Identify the parasite.
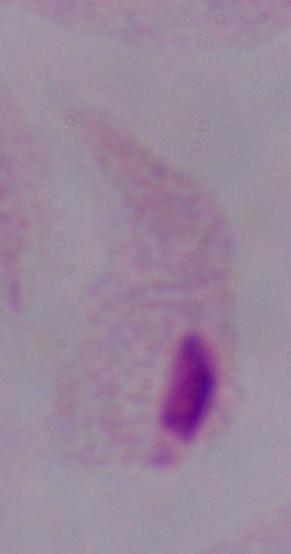

A trichomonad.

Captured at 1000x magnification. Photomicrograph.